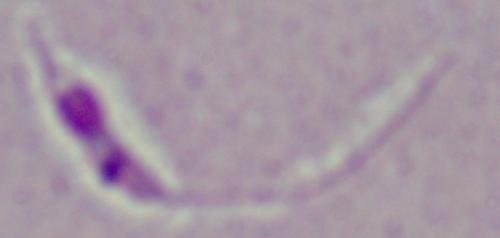
{
  "modality": "micrograph",
  "magnification": "1000x",
  "identification": "Leishmania"
}